Assess this cell for malaria.
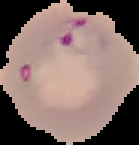

Parasitized.

image type = segmented cell region with the area outside set to black
image size = 139×145 pixels
preparation = thin blood film